Locate and identify every blood parasite.
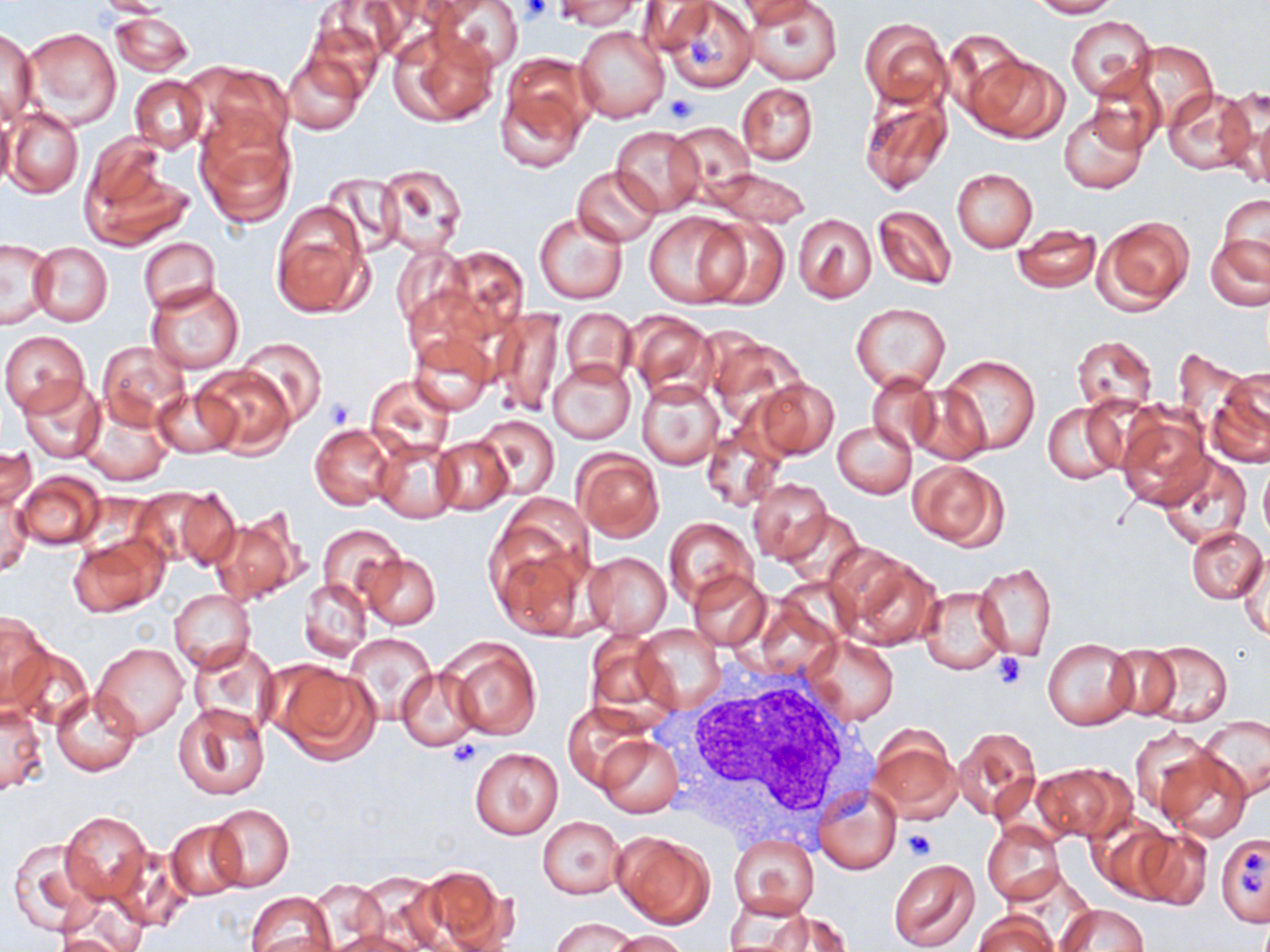

No blood parasites observed.

Summary:
  - Coordinate format: approximate bounding boxes as (x1,y1)-(x2,y2) corner pairs in pixels
  - Platelet locations: (521,0)-(552,24), (686,36)-(719,68), (665,93)-(696,124), (324,399)-(353,429), (994,653)-(1028,689), (447,740)-(482,768), (901,825)-(938,861), (1239,852)-(1264,890)
  - Uninfected red blood cell locations: (430,0)-(525,75), (555,0)-(640,30), (1028,0)-(1118,18), (319,1)-(413,64), (636,1)-(716,57), (662,2)-(756,92), (738,2)-(823,27), (748,2)-(841,85), (111,12)-(192,75), (1067,15)-(1157,101), (859,18)-(951,107), (299,20)-(384,104), (388,24)-(499,128), (574,26)-(669,124), (1,27)-(38,121), (21,27)-(122,129), (941,32)-(1037,124), (1133,41)-(1217,128), (283,51)-(365,135), (965,52)-(1070,144), (195,63)-(294,152), (496,63)-(591,170), (1088,71)-(1165,155), (130,75)-(208,152), (736,82)-(819,164), (1223,85)-(1270,189), (858,86)-(952,196), (1164,88)-(1254,174), (1058,106)-(1149,195), (6,109)-(82,198), (0,112)-(16,190), (195,120)-(297,228), (669,121)-(757,199), (611,125)-(705,216), (80,145)-(190,250), (374,163)-(468,257), (574,165)-(662,247), (704,168)-(812,228), (952,168)-(1037,252), (323,171)-(402,252), (1217,195)-(1270,280), (269,201)-(373,319), (873,205)-(957,291), (534,210)-(628,304), (643,211)-(746,308), (793,213)-(877,303), (1093,215)-(1194,313), (698,217)-(790,310), (1011,224)-(1102,293), (1207,234)-(1270,311), (1,237)-(56,330), (138,237)-(219,312), (29,243)-(112,325), (391,244)-(471,329), (443,246)-(529,335), (146,280)-(244,374), (403,285)-(497,374), (851,304)-(951,392), (489,307)-(566,417), (561,308)-(636,387), (625,310)-(719,403), (0,330)-(90,416), (408,334)-(494,415), (1072,336)-(1156,415), (238,338)-(327,427), (97,342)-(190,427), (940,354)-(1040,456), (547,358)-(635,444), (195,365)-(295,457), (1207,370)-(1270,468), (865,373)-(942,454), (364,375)-(454,461), (749,376)-(839,460), (16,377)-(105,463), (636,378)-(723,470), (905,384)-(991,464), (153,387)-(239,458), (79,399)-(173,486), (1041,399)-(1133,484), (1115,402)-(1212,508), (474,414)-(559,499), (832,419)-(917,498), (702,423)-(786,512), (311,424)-(394,509), (433,436)-(512,515), (372,439)-(461,522), (0,444)-(38,517), (573,449)-(664,540), (1153,451)-(1251,554), (908,460)-(1006,548), (1260,463)-(1270,543), (15,472)-(102,549), (748,478)-(832,563), (143,484)-(240,571), (0,488)-(32,576), (210,509)-(306,606), (777,511)-(863,588), (664,517)-(756,607), (319,523)-(404,606), (1186,526)-(1267,603), (67,536)-(165,617), (491,540)-(591,640), (582,550)-(672,638), (832,550)-(937,649), (359,552)-(440,630), (1238,554)-(1269,641), (975,562)-(1056,659), (688,568)-(772,650), (299,579)-(370,661), (920,586)-(1010,674), (167,589)-(254,674), (1,609)-(51,711), (635,624)-(725,713), (345,632)-(436,721), (585,633)-(669,715), (803,634)-(899,725), (443,638)-(541,739), (1042,639)-(1139,730), (188,640)-(280,735), (1141,640)-(1233,727), (92,644)-(189,740), (1106,644)-(1183,720), (3,645)-(93,730), (268,661)-(379,764), (396,667)-(482,751), (52,690)-(140,775), (172,701)-(269,801), (1,704)-(47,795), (563,704)-(653,790), (1197,717)-(1270,801), (1129,725)-(1212,814), (953,726)-(1042,820), (868,727)-(961,823), (595,735)-(682,819), (469,747)-(565,839), (1156,747)-(1251,840), (1034,764)-(1132,841), (815,783)-(900,873), (206,803)-(295,893), (60,811)-(151,903), (1089,815)-(1179,900), (537,817)-(625,897), (163,819)-(247,902), (981,820)-(1066,905), (538,822)-(704,911), (1133,828)-(1214,912), (611,829)-(716,928), (729,834)-(818,918), (1216,834)-(1270,927), (5,838)-(101,937), (106,843)-(193,933), (888,859)-(979,951), (418,864)-(514,952), (358,870)-(442,952), (309,881)-(385,947), (244,891)-(337,952), (724,898)-(816,950), (1059,903)-(1148,951), (762,909)-(851,950), (973,911)-(1055,952), (551,918)-(636,952), (327,929)-(425,952), (53,930)-(142,952), (608,930)-(688,951)
  - White blood cell locations: (680,671)-(879,842)
  - Slide-level diagnosis: negative for blood parasites
  - Image size: 1270×952 pixels
  - Field of view: single
  - Magnification: 1000x
  - Preparation: thin blood smear
  - Stain: May-Grünwald-Giemsa
  - Modality: light microscopy